State which parasite is depicted.
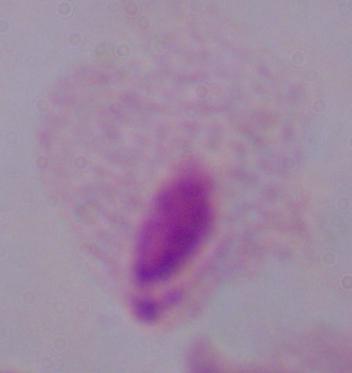

This is a trichomonad.

Summary:
  - Modality: photomicrograph
  - Magnification: 1000x